Classify this cell by malaria status.
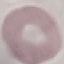

Uninfected.

Thin blood film. Cell patch, automatically extracted from a larger field of view and resized to 64 × 64 pixels. Acquired by smartphone through the microscope eyepiece. Giemsa-stained preparation.